Identify the blood parasite species.
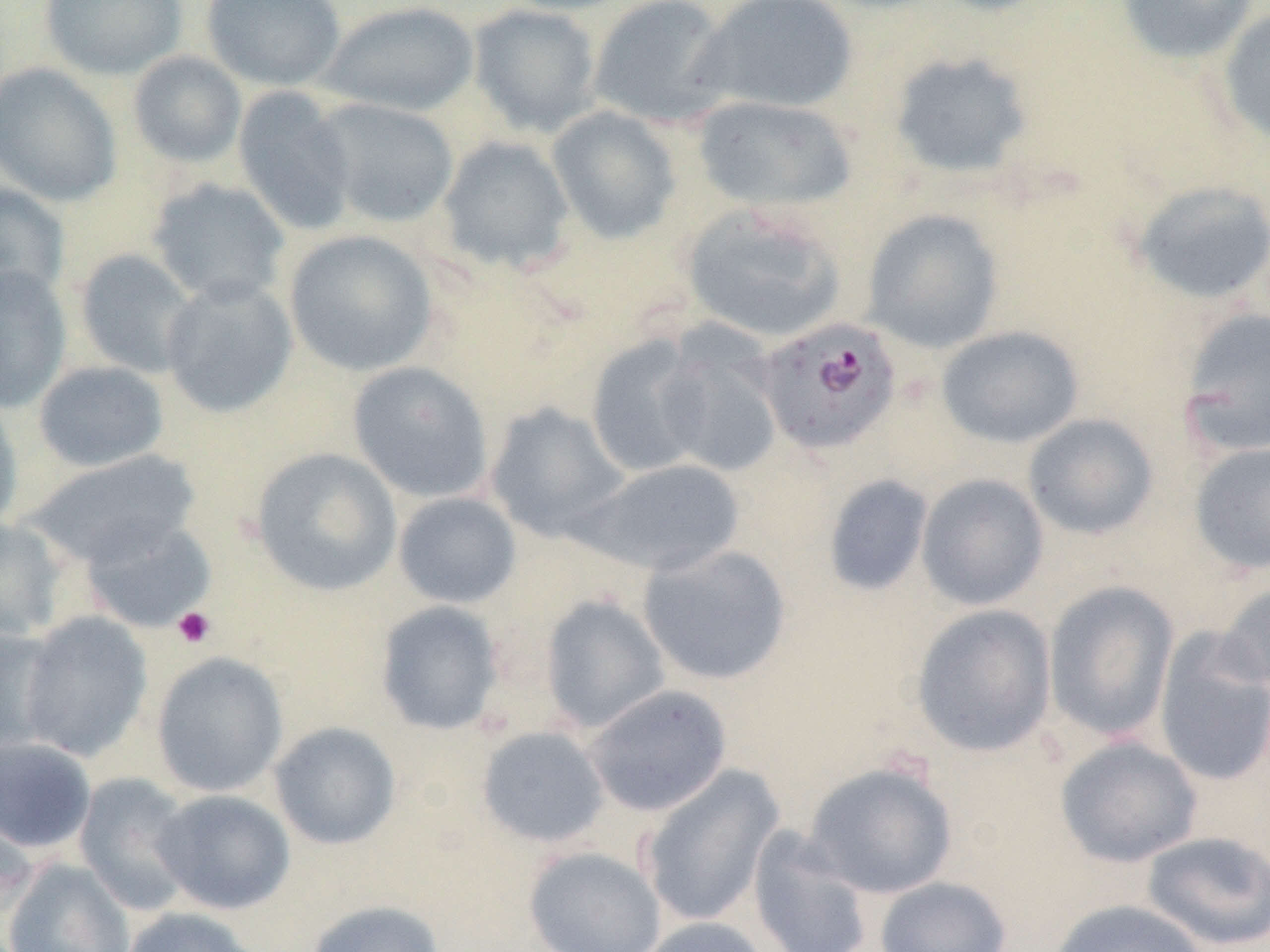
Plasmodium falciparum.

Approximate bounding boxes as (x1,y1)-(x2,y2) corner pairs in pixels. Platelet locations: (172,606)-(216,649). Plasmodium falciparum-infected red blood cell locations: (756,317)-(902,454). Uninfected red blood cell locations: (41,0)-(187,81), (201,0)-(346,91), (495,0)-(638,16), (587,0)-(735,129), (694,0)-(860,115), (925,0)-(1057,17), (1115,0)-(1260,65), (319,2)-(479,117), (468,3)-(602,137), (1216,9)-(1270,146), (127,50)-(247,169), (887,50)-(1036,183), (0,62)-(122,206), (233,86)-(357,236), (692,95)-(858,213), (312,98)-(459,228), (546,106)-(684,245), (436,136)-(575,275), (147,177)-(290,307), (1129,179)-(1270,306), (0,181)-(70,306), (680,201)-(848,344), (861,209)-(1004,354), (283,229)-(438,377), (74,249)-(201,379), (0,265)-(72,413), (160,277)-(298,419), (1179,307)-(1270,457), (936,325)-(1084,448), (585,334)-(712,479), (652,335)-(785,479), (33,360)-(169,472), (347,361)-(493,503), (0,393)-(23,533), (484,402)-(631,544), (1022,413)-(1159,540), (1188,441)-(1270,576), (250,447)-(403,597), (25,450)-(199,568), (577,458)-(746,577), (916,473)-(1049,611), (821,474)-(934,597), (392,492)-(522,609), (80,516)-(216,633), (0,517)-(68,641), (637,543)-(793,686), (1043,580)-(1180,742), (1216,580)-(1270,698), (539,594)-(671,733), (375,600)-(505,736), (911,604)-(1058,757), (18,612)-(152,762), (0,624)-(66,758), (1153,629)-(1270,787), (151,651)-(289,798), (584,684)-(733,817), (269,721)-(402,850), (476,726)-(609,848), (0,736)-(97,854), (1055,736)-(1203,868), (803,761)-(959,899), (638,764)-(785,929), (74,772)-(196,914), (152,789)-(296,915), (0,805)-(39,921), (748,826)-(874,952), (1140,831)-(1270,951), (523,846)-(666,951), (3,858)-(136,952), (874,876)-(1012,952), (1046,898)-(1210,952), (305,900)-(445,952), (120,906)-(265,952), (635,917)-(773,952). Single field of view. Thin blood film. Captured at 1000x magnification. Light microscopy. Image is 1270×952 pixels.